Locate every Plasmodium falciparum parasite and identify its life-cycle stage.
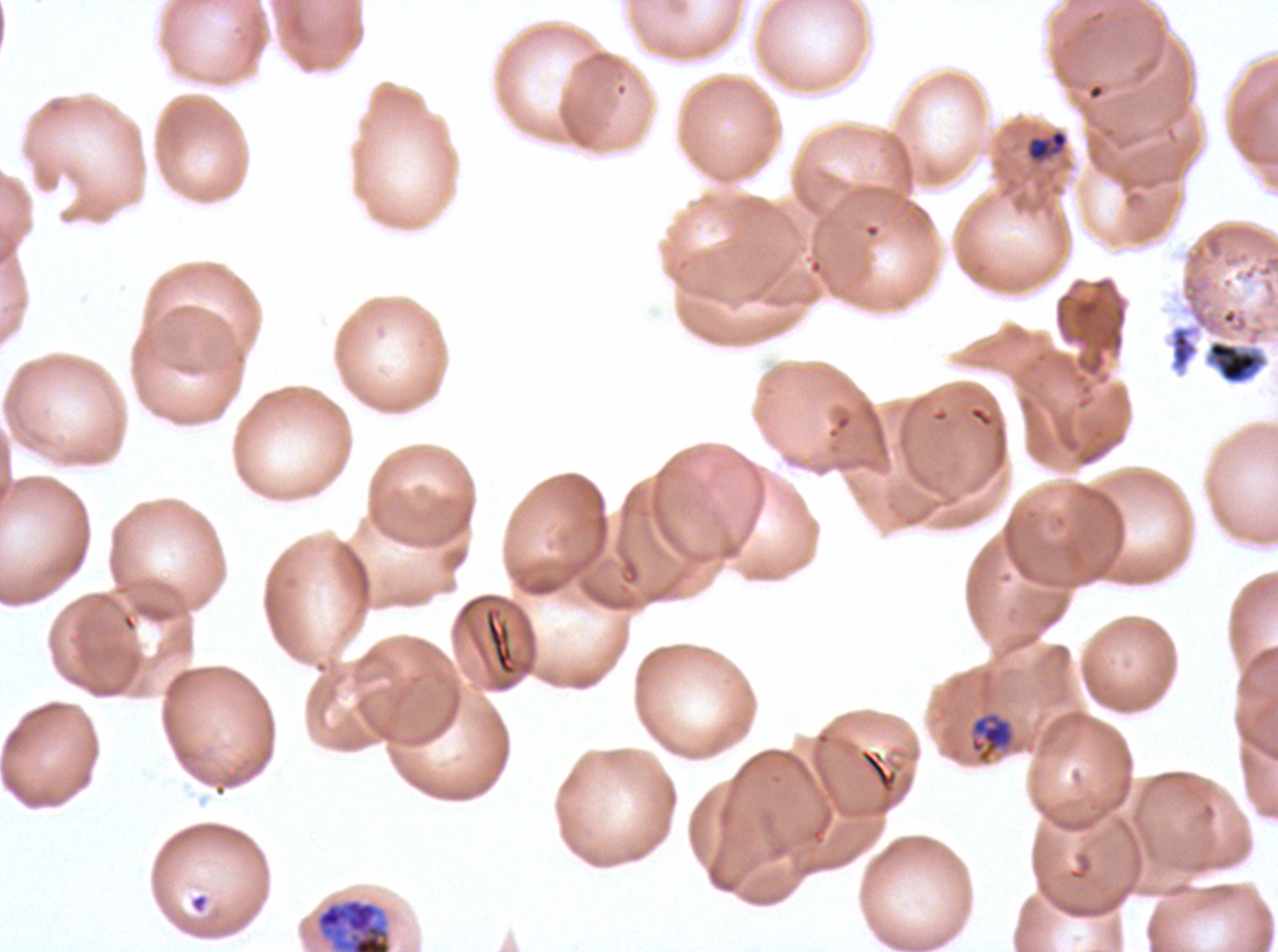
Approximate bounding rectangles given as corner coordinates in pixels from the top-left.
Late-ring/early-trophozoite forms: (x1=1026, y1=128, x2=1069, y2=164).
Mid trophozoites: (x1=969, y1=711, x2=1016, y2=764).
Early schizonts: (x1=315, y1=897, x2=392, y2=951).
No rings, late trophozoites, late schizonts, segmenters, or gametocytes observed.

Debris locations: (x1=1169, y1=324, x2=1199, y2=373), (x1=190, y1=893, x2=209, y2=914). Life-cycle stages observed: late-ring/early-trophozoite, mid trophozoite, early schizont. Giemsa-stained preparation. Image is 1278×952 pixels. Thin blood smear. Plasmodium falciparum cultured ex vivo for 24 to 48 hours, from a patient in The Gambia. A sub-image separated from a larger composite.